Comment on the morphology of the erythrocytes.
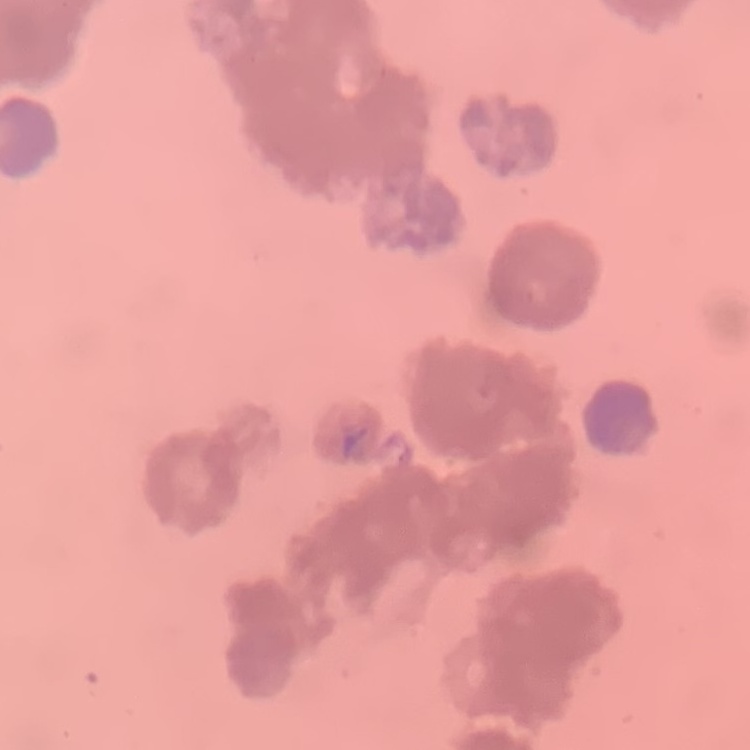

They show rouleaux formation.

Summary:
  - Image type: square crop of a larger photomicrograph
  - Stain: Field's or Giemsa
  - Preparation: thin peripheral smear